Locate every uninfected red blood cell.
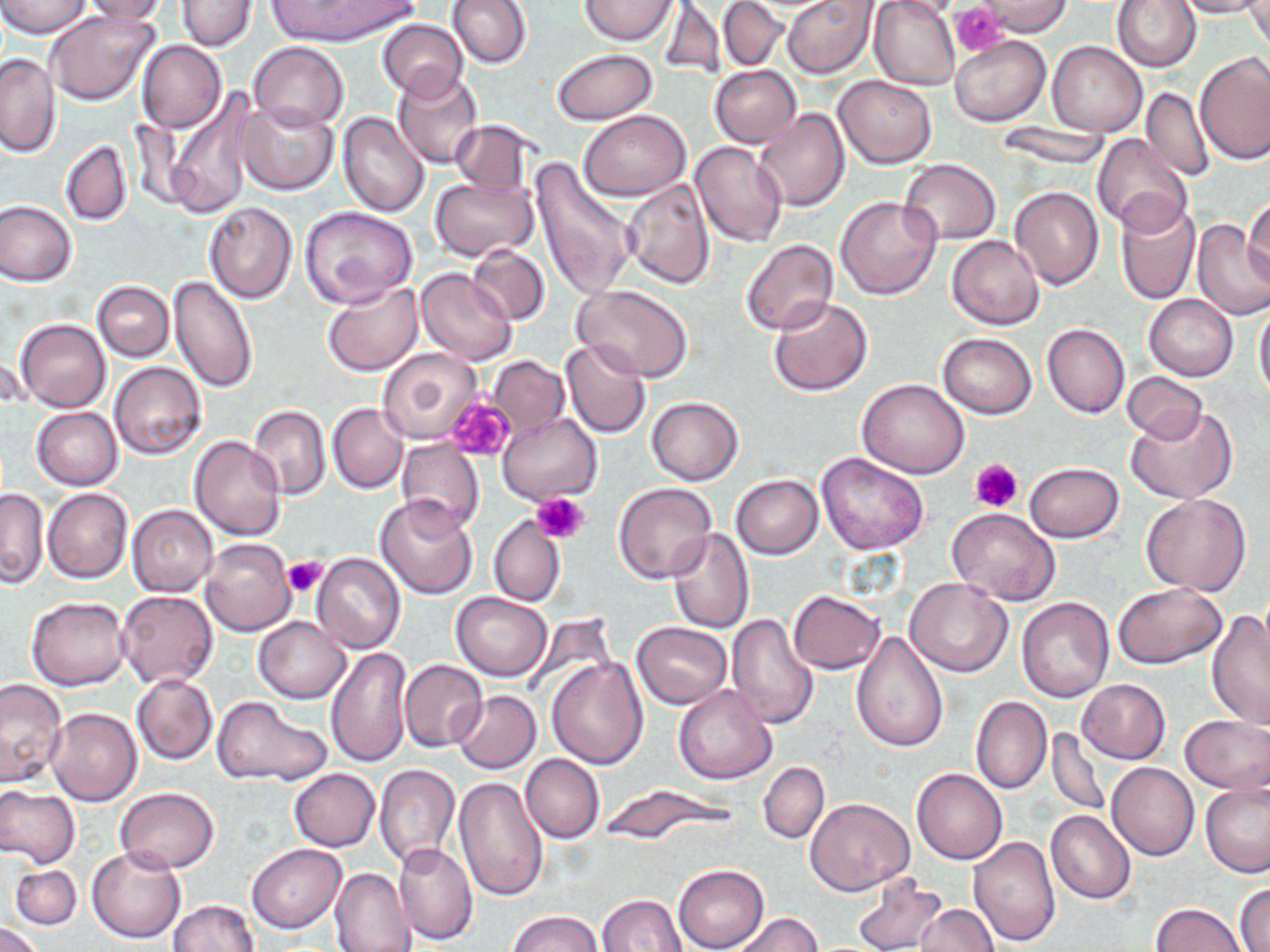
Approximate bounding boxes as [x1, y1, x2, y2] in pixels.
Uninfected red blood cells: [1, 0, 91, 37], [77, 0, 168, 23], [265, 0, 419, 47], [445, 0, 531, 69], [581, 0, 676, 45], [718, 0, 788, 71], [783, 0, 877, 77], [869, 0, 960, 91], [1112, 0, 1201, 73], [1175, 0, 1270, 18], [177, 1, 256, 51], [658, 1, 726, 84], [975, 1, 1074, 37], [1247, 2, 1270, 56], [46, 9, 160, 107], [381, 12, 533, 83], [376, 19, 468, 102], [951, 37, 1050, 125], [249, 41, 348, 131], [138, 42, 227, 132], [1047, 42, 1148, 137], [551, 49, 657, 125], [1196, 52, 1269, 164], [1, 53, 59, 157], [710, 65, 802, 148], [392, 68, 484, 170], [832, 75, 936, 169], [1140, 86, 1214, 182], [166, 93, 257, 220], [238, 101, 338, 195], [753, 108, 850, 213], [338, 111, 430, 217], [578, 111, 689, 200], [449, 120, 537, 196], [996, 122, 1110, 170], [1091, 134, 1194, 235], [60, 140, 133, 225], [689, 142, 788, 248], [529, 158, 635, 302], [898, 159, 1000, 245], [430, 176, 539, 260], [621, 177, 716, 289], [1009, 185, 1103, 289], [835, 197, 941, 301], [1244, 198, 1270, 287], [1116, 199, 1200, 306], [1, 201, 78, 286], [204, 201, 297, 303], [299, 207, 418, 309], [1193, 221, 1270, 321], [947, 235, 1043, 329], [740, 240, 837, 337], [465, 245, 550, 324], [415, 268, 517, 365], [168, 275, 260, 395], [93, 281, 173, 362], [323, 281, 423, 376], [571, 284, 694, 383], [1144, 294, 1238, 380], [767, 298, 873, 395], [1254, 302, 1270, 400], [15, 318, 111, 412], [1042, 323, 1130, 418], [939, 334, 1037, 418], [561, 338, 652, 439], [378, 347, 483, 444], [2, 351, 29, 411], [489, 356, 568, 433], [110, 361, 207, 460], [1122, 371, 1207, 443], [857, 377, 970, 478], [646, 396, 743, 485], [328, 402, 408, 494], [248, 404, 330, 500], [1126, 406, 1238, 504], [30, 407, 123, 490], [497, 411, 603, 504], [189, 436, 288, 540], [397, 440, 484, 535], [817, 452, 929, 555], [1023, 462, 1124, 543], [730, 474, 823, 558], [612, 483, 717, 585], [0, 487, 49, 587], [42, 487, 132, 584], [1140, 493, 1252, 596], [374, 495, 480, 599], [127, 505, 218, 596], [947, 508, 1060, 606], [489, 514, 565, 605], [666, 527, 754, 633], [200, 537, 296, 637], [312, 553, 406, 656], [905, 577, 1014, 678], [1113, 583, 1228, 669], [788, 590, 884, 674], [116, 591, 219, 689], [452, 593, 552, 681], [26, 596, 130, 691], [1017, 596, 1115, 702], [1205, 611, 1270, 730], [726, 613, 819, 729], [253, 617, 351, 704], [632, 623, 732, 708], [851, 631, 948, 753], [325, 644, 414, 769], [547, 656, 649, 768], [398, 659, 487, 752], [131, 674, 218, 764], [0, 677, 68, 790], [1076, 678, 1171, 764], [672, 684, 778, 785], [452, 690, 541, 774], [212, 695, 330, 788], [971, 695, 1051, 795], [46, 708, 142, 806], [1179, 715, 1270, 795], [1046, 727, 1110, 817], [521, 753, 604, 844], [758, 761, 829, 843], [1107, 763, 1199, 861], [375, 764, 460, 867], [289, 768, 380, 851], [911, 768, 1008, 864], [389, 774, 507, 887], [454, 775, 549, 901], [1200, 782, 1270, 877], [598, 784, 739, 842], [0, 786, 80, 868], [116, 787, 219, 872], [807, 798, 914, 896], [1046, 810, 1135, 905], [968, 834, 1060, 946], [394, 841, 478, 945], [246, 844, 346, 933], [86, 845, 186, 944], [674, 864, 769, 952], [10, 865, 82, 930], [330, 868, 416, 952], [849, 870, 948, 952], [1234, 883, 1269, 952], [596, 894, 688, 952], [169, 900, 259, 952], [1152, 902, 1248, 952], [915, 904, 1001, 951], [506, 910, 604, 952], [732, 913, 822, 952], [1, 922, 43, 952].

{
  "slide_level_diagnosis": "negative for blood parasites",
  "platelet_locations": "approximate bounding boxes as [x1, y1, x2, y2] in pixels: [953, 4, 1007, 55], [445, 398, 515, 462], [970, 457, 1023, 512], [531, 492, 589, 545], [282, 555, 328, 597]",
  "stain": "May-Grünwald-Giemsa",
  "preparation": "thin blood film",
  "magnification": "1000x",
  "image_size": "1270×952 pixels",
  "modality": "light microscopy",
  "field_of_view": "single"
}